Identify the preparation type.
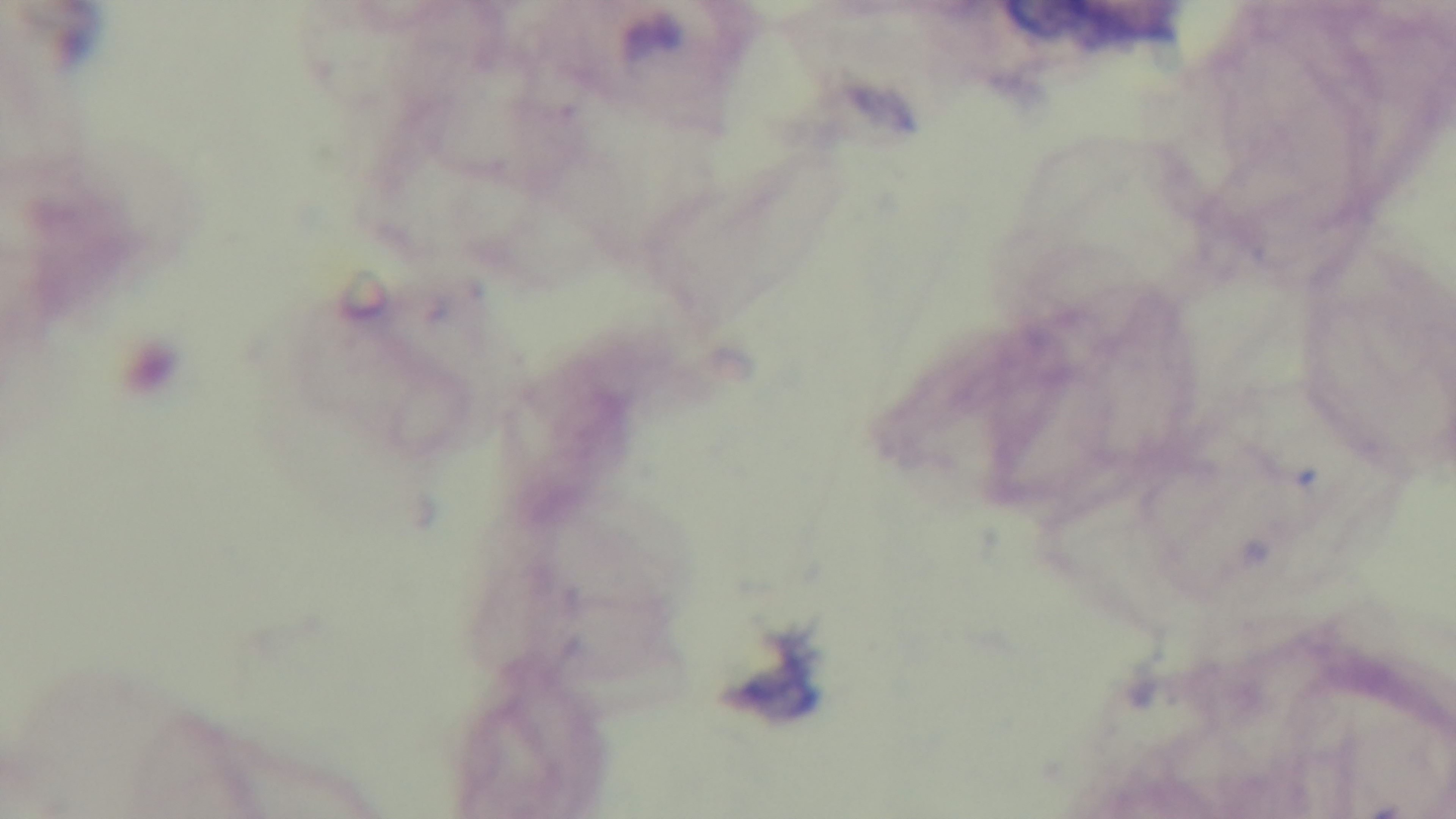
It is a thick blood film.

capture = mounted 4K digital camera
objective = 100x oil immersion
stain = Giemsa
malaria status = uninfected
field of view = one from the slide
modality = light microscopy